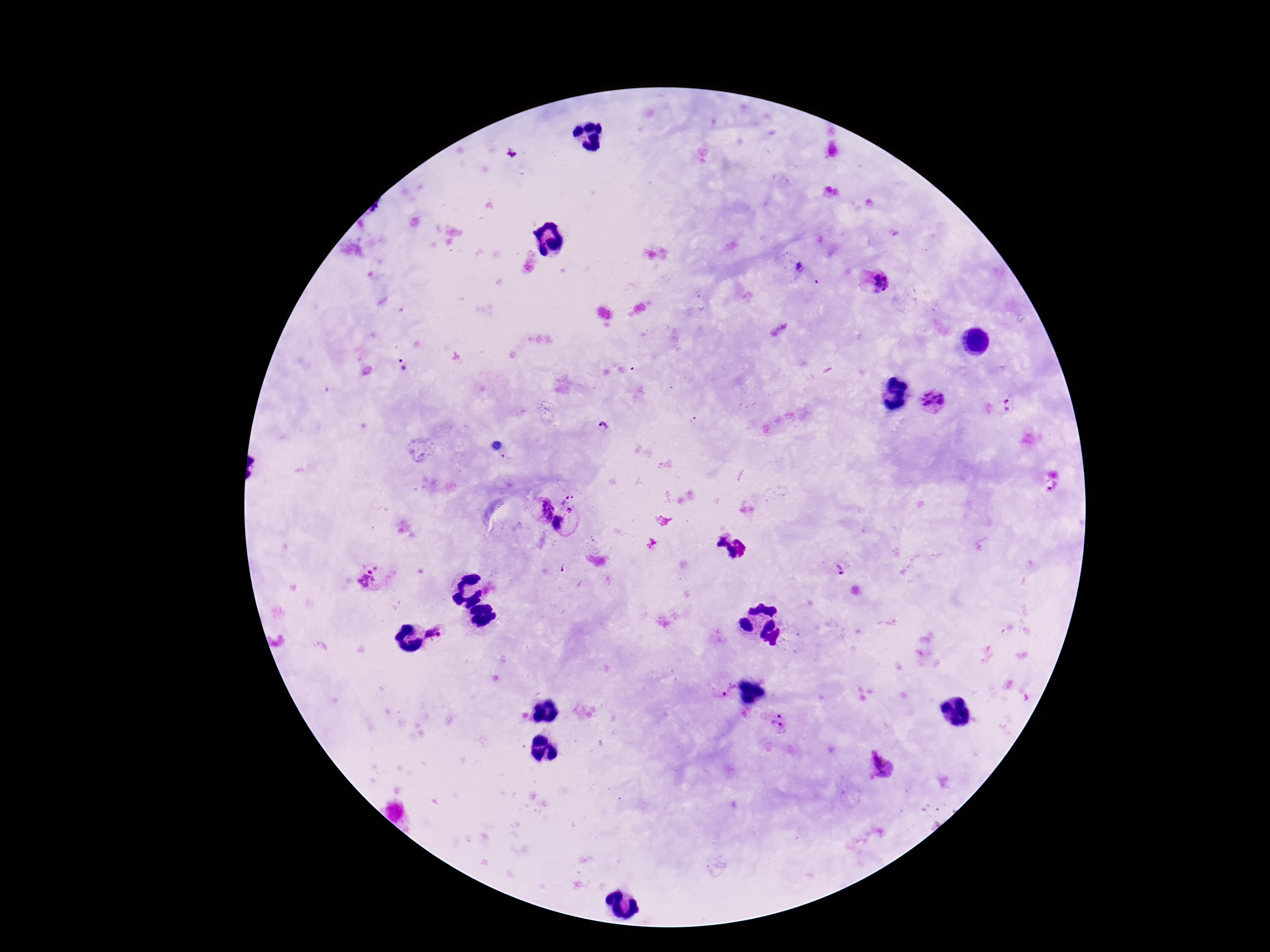
stain: Giemsa
capture: smartphone camera through the microscope eyepiece
patient_malaria_status: infected
preparation: thick blood smear
magnification: 100x
image_size: 1270×952 pixels
plasmodium_parasite_locations: 'approximate centers as [x, y] in pixels: [510, 154], [801, 268], [874, 283], [403, 366], [933, 401], [1009, 402], [604, 428], [564, 499], [542, 509], [570, 510], [559, 523], [842, 568], [368, 578], [433, 634], [729, 689], [774, 717], [781, 729], [881, 768]'
field_of_view: single